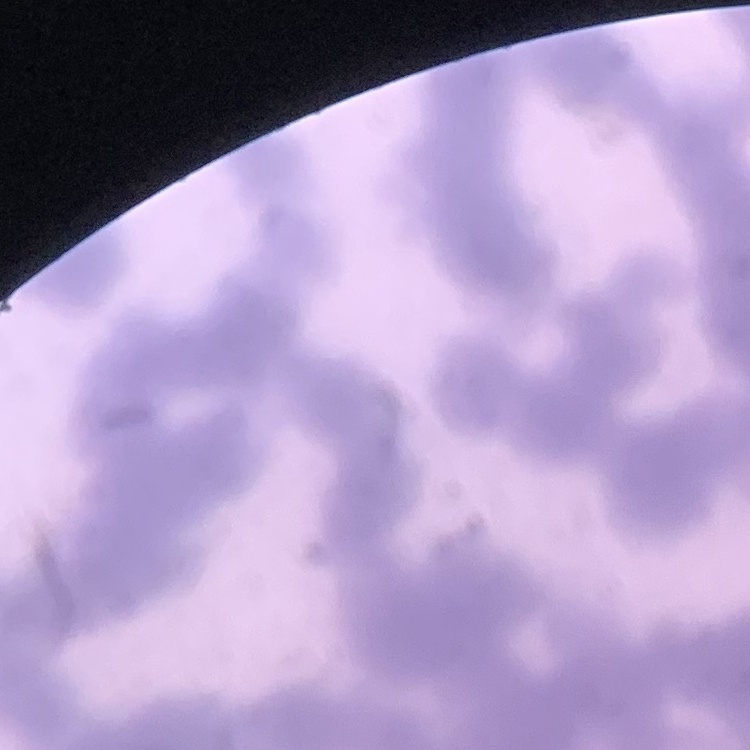 The red blood cells show rouleaux formation. Stained with either Field's or Giemsa. Thin blood smear. One tile cut from a larger photomicrograph.